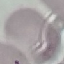
result = no malaria parasites seen
capture = smartphone through the microscope eyepiece
stain = Giemsa
image type = cell patch, automatically extracted from a larger field of view and resized to 64 × 64 pixels
preparation = thin blood film